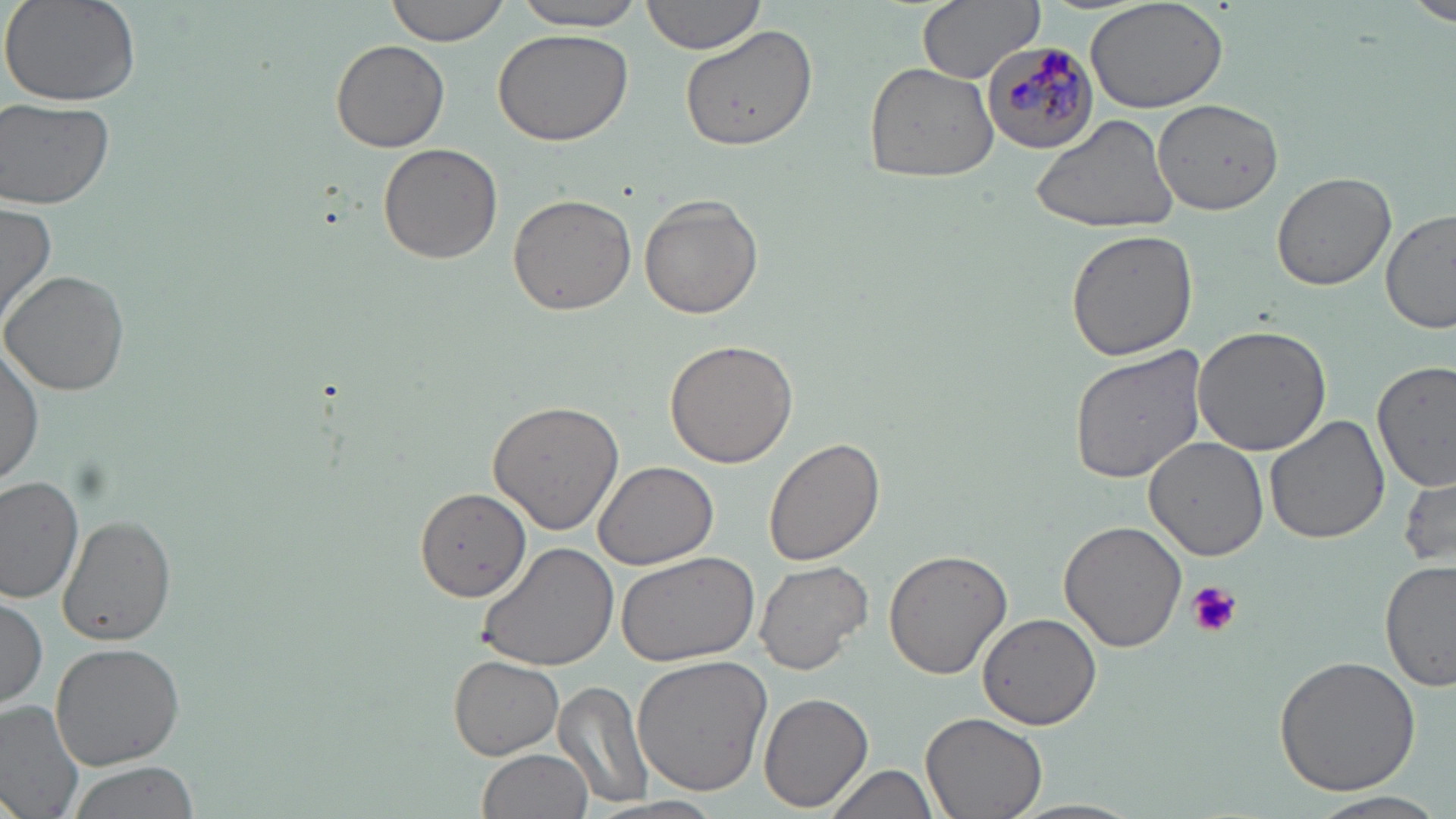

Approximate bounding boxes as (x1,y1)-(x2,y2) corner pairs in pixels. Plasmodium malariae-infected red blood cell locations: (980,39)-(1099,154). Platelet locations: (1185,581)-(1240,638). Uninfected red blood cell locations: (2,0)-(142,109), (385,0)-(516,46), (639,0)-(768,55), (915,0)-(1045,82), (1085,0)-(1231,114), (1410,0)-(1456,28), (508,1)-(649,30), (492,27)-(633,146), (681,27)-(819,153), (331,37)-(451,153), (863,60)-(999,184), (1151,99)-(1283,213), (1,100)-(115,209), (1029,112)-(1178,236), (377,143)-(502,265), (1271,172)-(1396,292), (508,192)-(636,316), (639,195)-(764,319), (0,198)-(59,333), (1379,208)-(1456,336), (1065,229)-(1200,360), (1,268)-(132,395), (1192,322)-(1334,454), (0,337)-(44,491), (665,339)-(800,468), (1067,344)-(1207,484), (1374,361)-(1455,488), (487,400)-(625,535), (1264,414)-(1389,545), (1141,435)-(1271,561), (764,438)-(886,566), (591,461)-(717,569), (1399,472)-(1456,567), (0,475)-(86,603), (413,487)-(530,605), (59,515)-(176,647), (1057,520)-(1188,654), (473,541)-(620,671), (614,550)-(760,668), (883,550)-(1011,681), (754,559)-(873,677), (1380,560)-(1456,693), (0,592)-(48,709), (977,611)-(1104,730), (51,640)-(187,770), (632,653)-(773,797), (1272,654)-(1422,798), (447,655)-(563,759), (552,682)-(655,810), (757,693)-(874,812), (0,700)-(85,819), (920,711)-(1047,819), (478,748)-(594,819), (66,761)-(202,818), (825,762)-(943,819), (1304,790)-(1453,817), (594,796)-(728,819), (1009,797)-(1148,819). Slide-level diagnosis: Plasmodium malariae. Single field of view. Light microscopy. May-Grünwald-Giemsa stain. Image is 1456×819 pixels. Thin blood smear. 1000x magnification.